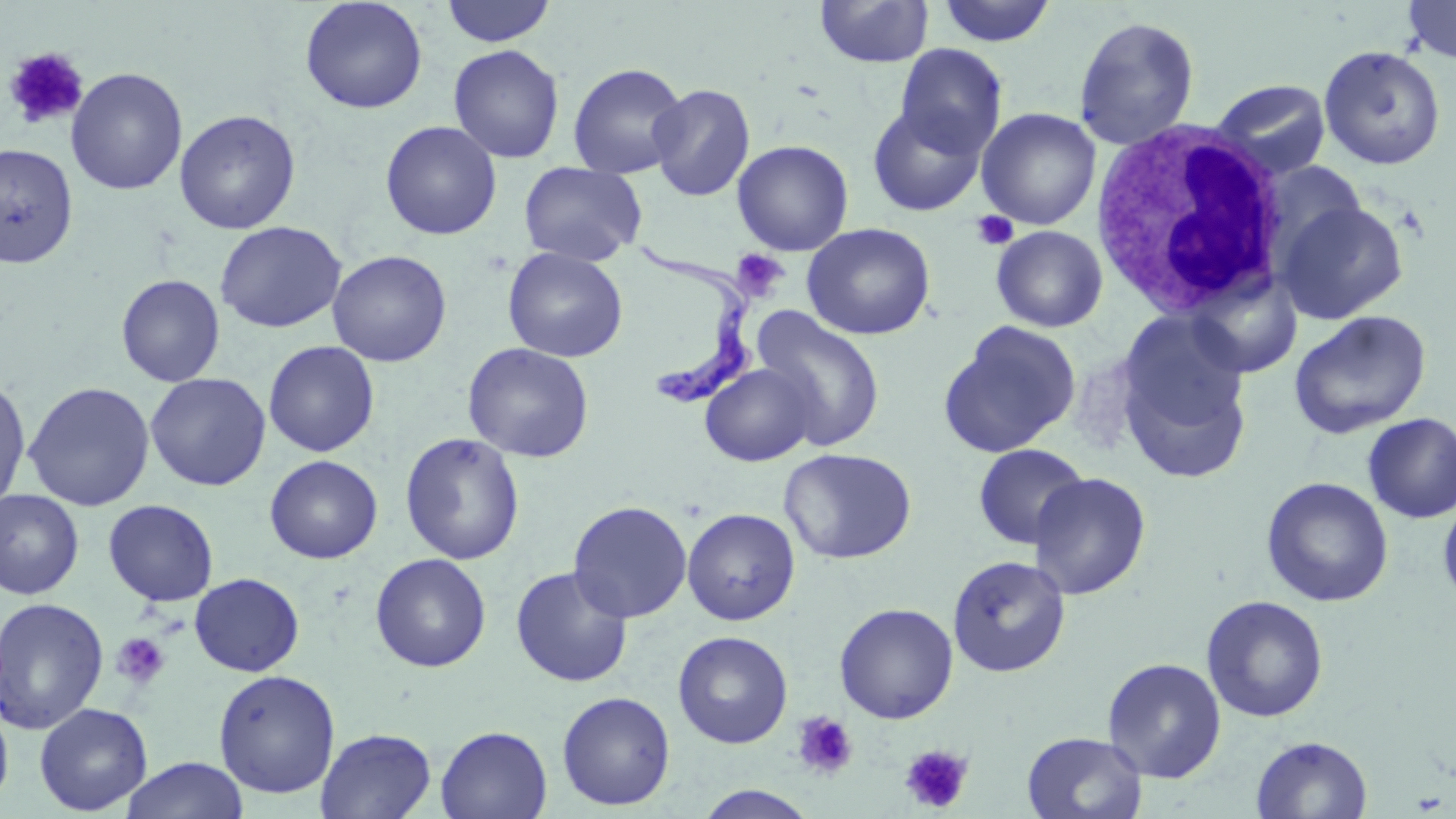
Summary:
  - Coordinate format: approximate bounding boxes as (x1, y1, x2, y2) in pixels
  - Uninfected red blood cell locations: (300, 0, 428, 114), (440, 0, 557, 47), (815, 0, 934, 68), (935, 0, 1058, 47), (1401, 0, 1456, 64), (1073, 15, 1200, 150), (448, 44, 565, 163), (894, 44, 1008, 158), (1319, 45, 1446, 170), (568, 62, 689, 178), (65, 67, 187, 196), (1209, 79, 1332, 180), (648, 83, 756, 202), (867, 103, 988, 216), (976, 107, 1101, 230), (174, 109, 301, 234), (380, 120, 502, 240), (732, 139, 854, 256), (0, 142, 78, 268), (518, 162, 646, 266), (1276, 199, 1409, 324), (215, 221, 346, 333), (802, 223, 936, 340), (991, 225, 1108, 332), (503, 247, 628, 362), (327, 250, 451, 367), (1186, 267, 1304, 379), (116, 274, 225, 387), (750, 306, 886, 451), (1288, 310, 1432, 439), (939, 321, 1081, 458), (1116, 333, 1254, 483), (263, 340, 380, 457), (462, 342, 594, 463), (700, 362, 818, 466), (145, 372, 271, 491), (0, 376, 31, 511), (23, 381, 155, 511), (1362, 413, 1456, 522), (399, 432, 525, 566), (973, 443, 1090, 550), (779, 448, 917, 564), (264, 454, 382, 564), (1028, 472, 1151, 600), (1260, 477, 1394, 607), (0, 490, 84, 600), (1438, 494, 1456, 609), (103, 499, 218, 606), (568, 500, 692, 623), (682, 508, 800, 625), (370, 553, 491, 672), (947, 554, 1071, 678), (510, 566, 633, 688), (190, 573, 304, 676), (1201, 595, 1328, 722), (0, 596, 109, 735), (834, 603, 959, 724), (673, 630, 793, 749), (1102, 657, 1226, 782), (213, 669, 341, 798), (556, 691, 676, 810), (0, 694, 14, 811), (34, 702, 153, 816), (436, 725, 552, 819), (315, 727, 437, 818), (1022, 731, 1148, 819), (1251, 735, 1373, 819), (120, 757, 250, 819), (693, 785, 821, 819)
  - White blood cell locations: (1091, 119, 1291, 320)
  - Platelet locations: (3, 46, 89, 130), (971, 211, 1018, 252), (731, 248, 789, 300), (111, 631, 172, 691), (791, 711, 858, 780), (901, 744, 974, 814)
  - Trypanosoma brucei locations: (635, 235, 764, 409)
  - Slide-level diagnosis: Trypanosoma brucei
  - Modality: light microscopy
  - Magnification: 1000x
  - Image size: 1456×819 pixels
  - Stain: May-Grünwald-Giemsa
  - Preparation: thin blood film
  - Field of view: single